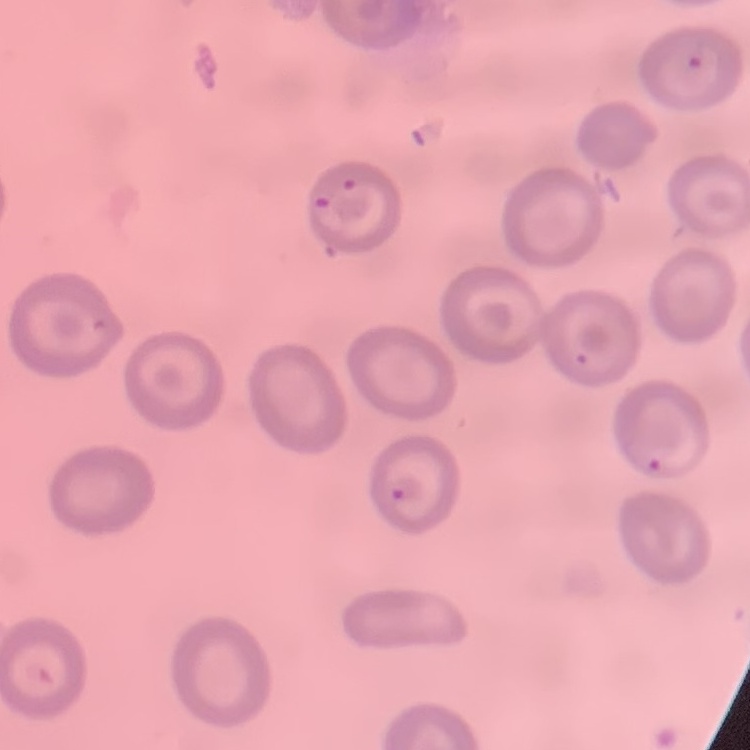
The erythrocytes exhibit no rouleaux formation. One tile cut from a larger photomicrograph. Thin blood smear. Stained with either Field's or Giemsa.